State the blood parasite species.
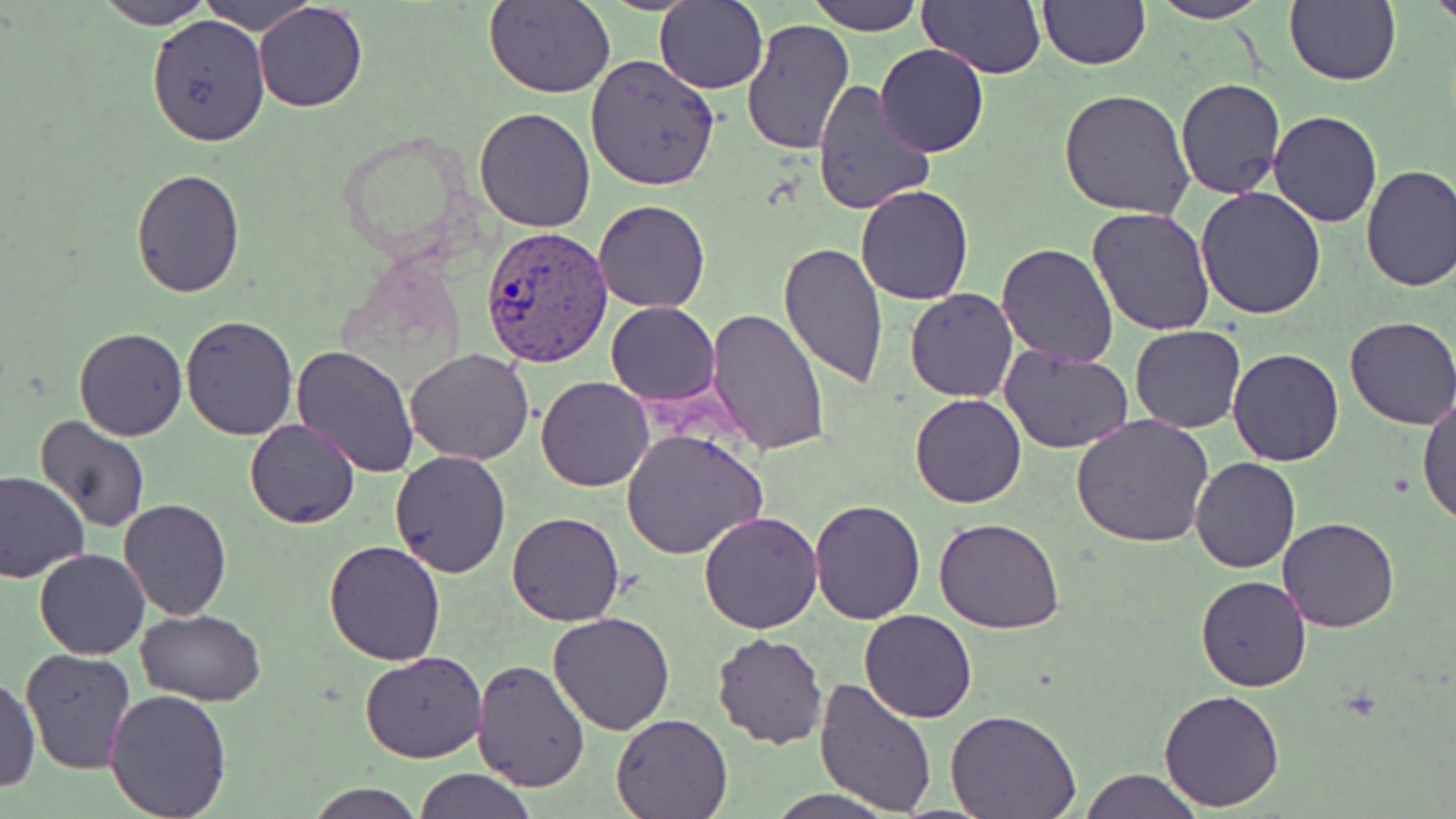
Plasmodium vivax.

Approximate bounding boxes as [x1, y1, x2, y2] in pixels. Plasmodium vivax-infected red blood cell locations: [480, 225, 613, 368]. Uninfected red blood cell locations: [198, 0, 315, 33], [484, 0, 616, 98], [809, 0, 925, 35], [917, 0, 1044, 78], [1148, 0, 1270, 24], [1284, 0, 1400, 85], [1427, 0, 1456, 33], [94, 1, 214, 29], [654, 1, 768, 91], [1038, 1, 1150, 69], [253, 2, 368, 112], [148, 14, 271, 146], [739, 18, 854, 157], [875, 44, 989, 159], [585, 55, 720, 192], [810, 78, 936, 218], [1175, 78, 1287, 200], [1059, 89, 1195, 219], [475, 107, 596, 231], [1267, 110, 1383, 228], [1360, 164, 1456, 293], [131, 170, 244, 297], [856, 185, 974, 305], [1195, 186, 1328, 320], [592, 200, 709, 313], [1087, 206, 1218, 336], [996, 242, 1119, 367], [778, 243, 890, 387], [904, 288, 1018, 402], [605, 300, 719, 404], [705, 306, 833, 456], [180, 314, 300, 439], [1344, 317, 1456, 428], [1129, 326, 1247, 433], [74, 327, 188, 441], [1000, 345, 1132, 455], [292, 346, 418, 478], [1227, 347, 1345, 465], [405, 348, 534, 464], [536, 376, 654, 491], [1418, 391, 1456, 528], [910, 393, 1028, 508], [1071, 414, 1214, 548], [33, 415, 155, 534], [245, 419, 360, 528], [620, 428, 769, 562], [388, 450, 511, 577], [1190, 456, 1300, 572], [0, 470, 90, 583], [118, 499, 232, 621], [810, 499, 925, 624], [698, 509, 823, 633], [506, 511, 627, 626], [934, 517, 1065, 634], [1278, 517, 1399, 633], [324, 539, 448, 665], [34, 548, 152, 660], [1195, 574, 1313, 692], [137, 609, 267, 705], [860, 610, 976, 724], [547, 611, 677, 734], [712, 632, 829, 749], [21, 649, 136, 772], [360, 651, 487, 763], [471, 658, 592, 793], [1, 673, 41, 793], [813, 674, 941, 814], [104, 689, 232, 817], [1159, 690, 1286, 812], [944, 710, 1080, 818], [611, 713, 730, 818], [415, 769, 534, 819], [1080, 769, 1201, 819], [307, 782, 423, 819], [770, 791, 892, 819]. Image is 1456×819 pixels. Thin blood film. Light microscopy. 1000x magnification. May-Grünwald-Giemsa stain. One field of a larger specimen.